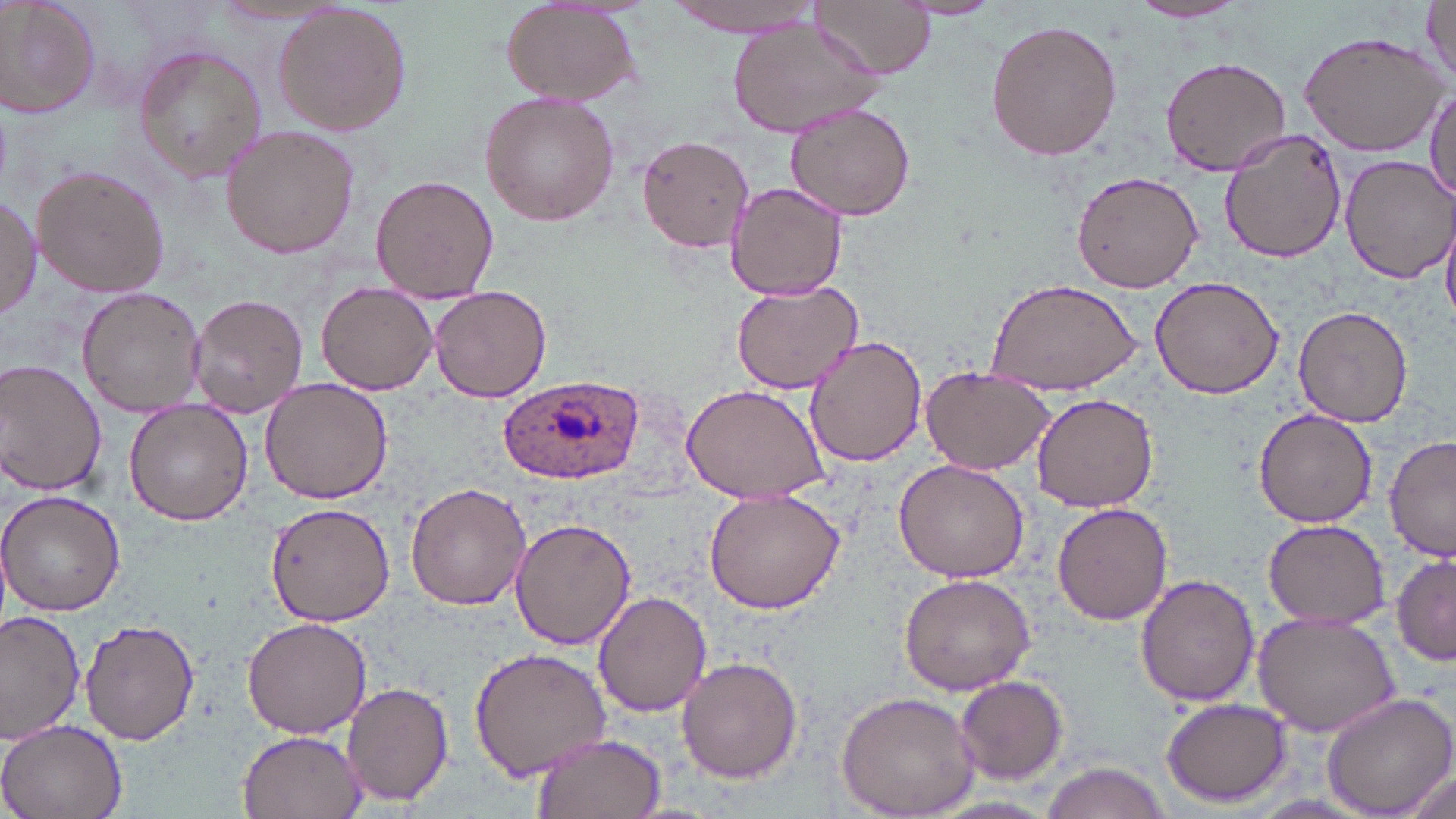
slide_level_diagnosis: Plasmodium ovale
stain: May-Grünwald-Giemsa
magnification: 1000x
plasmodium_ovale_infected_red_blood_cell_locations: 'approximate bounding boxes as named x1/y1/x2/y2 corners in pixels: (x1=498, y1=376, x2=641, y2=485)'
image_size: 1456×819 pixels
uninfected_red_blood_cell_locations: 'approximate bounding boxes as named x1/y1/x2/y2 corners in pixels: (x1=0, y1=0, x2=101, y2=118), (x1=810, y1=0, x2=934, y2=80), (x1=900, y1=0, x2=1004, y2=20), (x1=1423, y1=0, x2=1456, y2=89), (x1=665, y1=1, x2=823, y2=34), (x1=1130, y1=1, x2=1249, y2=23), (x1=501, y1=2, x2=641, y2=105), (x1=271, y1=4, x2=412, y2=135), (x1=726, y1=15, x2=885, y2=137), (x1=986, y1=18, x2=1125, y2=162), (x1=1297, y1=29, x2=1448, y2=156), (x1=132, y1=43, x2=267, y2=182), (x1=1160, y1=56, x2=1290, y2=175), (x1=1427, y1=83, x2=1456, y2=204), (x1=481, y1=92, x2=620, y2=227), (x1=783, y1=101, x2=916, y2=221), (x1=219, y1=125, x2=360, y2=259), (x1=1219, y1=129, x2=1348, y2=264), (x1=635, y1=135, x2=755, y2=253), (x1=1338, y1=154, x2=1456, y2=283), (x1=33, y1=165, x2=169, y2=299), (x1=1071, y1=168, x2=1204, y2=294), (x1=371, y1=175, x2=497, y2=302), (x1=724, y1=180, x2=851, y2=299), (x1=0, y1=194, x2=42, y2=320), (x1=1442, y1=214, x2=1456, y2=326), (x1=1150, y1=275, x2=1284, y2=398), (x1=985, y1=278, x2=1142, y2=393), (x1=730, y1=280, x2=862, y2=393), (x1=317, y1=281, x2=437, y2=394), (x1=430, y1=285, x2=552, y2=402), (x1=76, y1=287, x2=206, y2=416), (x1=189, y1=293, x2=307, y2=419), (x1=1292, y1=304, x2=1413, y2=428), (x1=805, y1=335, x2=928, y2=466), (x1=0, y1=360, x2=107, y2=496), (x1=920, y1=364, x2=1057, y2=476), (x1=259, y1=377, x2=391, y2=505), (x1=679, y1=383, x2=828, y2=504), (x1=1031, y1=393, x2=1159, y2=512), (x1=124, y1=397, x2=254, y2=525), (x1=1253, y1=409, x2=1380, y2=528), (x1=1384, y1=435, x2=1456, y2=560), (x1=894, y1=459, x2=1030, y2=583), (x1=405, y1=481, x2=530, y2=610), (x1=703, y1=486, x2=845, y2=613), (x1=0, y1=489, x2=126, y2=615), (x1=265, y1=501, x2=395, y2=627), (x1=1054, y1=502, x2=1174, y2=625), (x1=509, y1=517, x2=635, y2=650), (x1=1263, y1=519, x2=1389, y2=629), (x1=1390, y1=547, x2=1454, y2=666), (x1=897, y1=573, x2=1037, y2=696), (x1=1136, y1=573, x2=1259, y2=707), (x1=591, y1=591, x2=712, y2=716), (x1=0, y1=610, x2=85, y2=742), (x1=1254, y1=610, x2=1401, y2=737), (x1=243, y1=615, x2=371, y2=739), (x1=81, y1=618, x2=199, y2=745), (x1=468, y1=645, x2=613, y2=782), (x1=675, y1=656, x2=803, y2=785), (x1=955, y1=674, x2=1068, y2=783), (x1=341, y1=681, x2=453, y2=808), (x1=835, y1=691, x2=981, y2=818), (x1=1321, y1=691, x2=1456, y2=819), (x1=1160, y1=696, x2=1294, y2=806), (x1=0, y1=718, x2=129, y2=819), (x1=237, y1=730, x2=365, y2=818), (x1=532, y1=732, x2=665, y2=819), (x1=1039, y1=762, x2=1173, y2=818), (x1=1391, y1=766, x2=1454, y2=819)'
preparation: thin blood smear
field_of_view: single
modality: optical microscopy